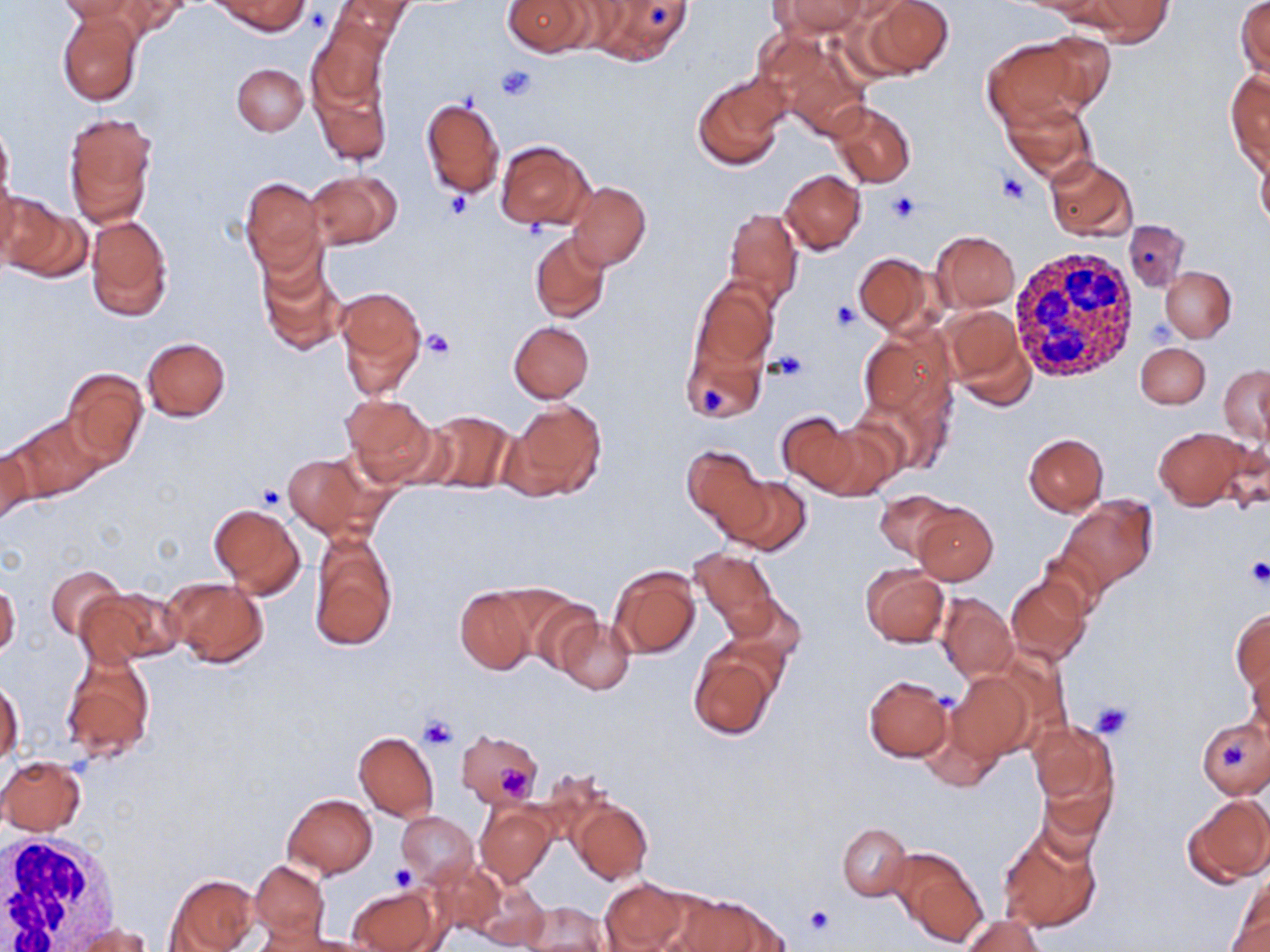

Approximate bounding boxes as [x1, y1, x2, y2] in pixels. White blood cell locations: [1008, 246, 1140, 380], [0, 830, 121, 952]. Uninfected red blood cell locations: [57, 0, 148, 24], [110, 0, 192, 37], [214, 0, 308, 36], [327, 0, 415, 50], [502, 0, 594, 55], [584, 0, 697, 63], [772, 0, 869, 36], [862, 0, 953, 78], [1080, 0, 1173, 44], [1236, 0, 1270, 80], [57, 8, 145, 106], [308, 21, 390, 115], [757, 27, 872, 141], [1032, 31, 1118, 111], [982, 38, 1091, 127], [310, 59, 392, 167], [232, 63, 308, 135], [1225, 70, 1270, 173], [693, 75, 788, 170], [419, 98, 505, 200], [1001, 99, 1094, 183], [829, 101, 916, 188], [63, 113, 157, 227], [0, 119, 15, 212], [495, 140, 594, 230], [1257, 147, 1270, 235], [1043, 155, 1136, 241], [307, 170, 401, 250], [780, 170, 866, 254], [240, 177, 325, 276], [567, 180, 651, 271], [2, 196, 88, 283], [724, 207, 803, 309], [86, 214, 173, 322], [1122, 219, 1190, 293], [931, 231, 1020, 311], [528, 232, 610, 323], [257, 248, 347, 357], [853, 252, 936, 336], [1161, 267, 1236, 341], [690, 279, 778, 375], [335, 288, 428, 396], [940, 304, 1034, 405], [509, 322, 593, 402], [860, 328, 955, 418], [141, 336, 231, 421], [681, 338, 767, 425], [1135, 343, 1210, 409], [1217, 363, 1269, 447], [61, 366, 148, 469], [341, 394, 437, 484], [505, 400, 608, 501], [420, 409, 516, 494], [775, 411, 869, 493], [7, 412, 106, 502], [808, 421, 903, 500], [1153, 426, 1251, 510], [1024, 433, 1109, 516], [0, 445, 35, 526], [683, 447, 770, 539], [283, 455, 367, 535], [725, 476, 811, 556], [876, 490, 956, 559], [1058, 497, 1158, 592], [209, 504, 305, 598], [912, 504, 998, 586], [310, 534, 398, 651], [1038, 543, 1114, 618], [689, 547, 779, 638], [608, 564, 702, 659], [45, 565, 124, 641], [861, 565, 949, 646], [1006, 575, 1091, 664], [164, 577, 268, 668], [0, 582, 21, 659], [78, 586, 182, 667], [454, 587, 537, 674], [515, 590, 604, 674], [937, 593, 1018, 681], [725, 594, 807, 669], [1232, 608, 1269, 695], [555, 617, 635, 693], [688, 644, 782, 739], [60, 651, 156, 761], [1246, 655, 1269, 743], [947, 671, 1034, 762], [863, 675, 954, 762], [0, 678, 24, 767], [922, 708, 1002, 792], [1196, 719, 1269, 797], [1028, 721, 1119, 814], [456, 728, 544, 808], [353, 731, 439, 819], [0, 756, 85, 835], [1034, 760, 1116, 857], [283, 793, 377, 877], [1184, 793, 1270, 884], [568, 797, 652, 885], [476, 803, 556, 887], [397, 812, 478, 883], [837, 823, 913, 900], [998, 825, 1103, 933], [893, 848, 986, 947], [250, 861, 330, 944], [426, 861, 507, 936], [167, 875, 257, 952], [1231, 876, 1270, 949], [598, 877, 689, 952], [475, 883, 552, 948], [349, 886, 443, 952], [678, 896, 789, 951], [519, 902, 610, 950], [962, 914, 1044, 952], [70, 923, 151, 952], [276, 932, 378, 951]. Platelet locations: [305, 5, 331, 33], [495, 64, 537, 101], [998, 172, 1029, 206], [443, 191, 473, 222], [886, 191, 922, 223], [831, 299, 859, 330], [1146, 319, 1178, 348], [425, 329, 455, 361], [770, 350, 809, 382], [696, 384, 725, 419], [257, 484, 287, 509], [1244, 557, 1270, 588], [1090, 701, 1132, 738], [419, 715, 460, 751], [1221, 741, 1248, 772], [495, 762, 531, 796], [388, 864, 415, 889], [805, 904, 835, 936]. Slide-level diagnosis: no evidence of blood parasites. Image is 1270×952 pixels. Optical microscopy. One field of a larger specimen. Thin blood film. Captured at 1000x magnification. May-Grünwald-Giemsa-stained preparation.